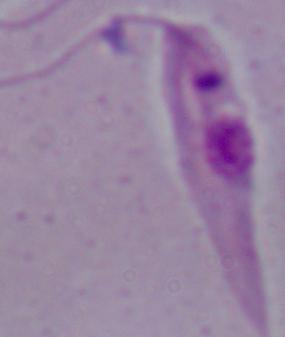
Summary:
  - Identification: Leishmania
  - Magnification: 1000x
  - Modality: micrograph